Comment on the morphology of the erythrocytes.
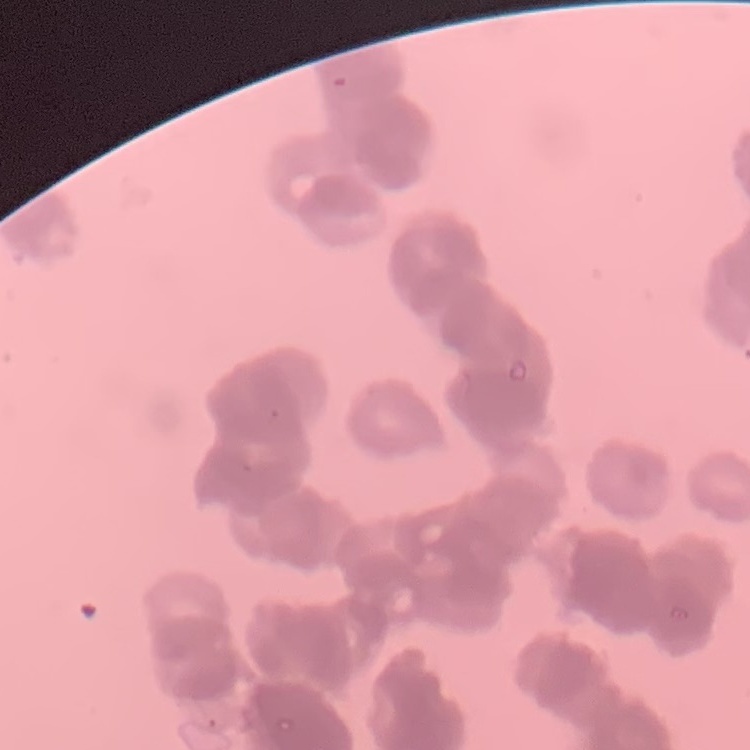

Rouleaux formation.

Summary:
  - Stain: Field's or Giemsa
  - Preparation: thin blood film
  - Image type: square crop of a larger photomicrograph